Report the malaria status of this cell.
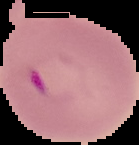

Parasitized.

Summary:
  - Image size: 139×145 pixels
  - Image type: cell region segmented out of the field of view; surrounding area masked to black
  - Preparation: thin blood film